Identify the parasite.
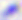
Toxoplasma gondii.

Photomicrograph. Captured at 400x magnification.